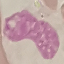

result = negative for malaria parasites
stain = Giemsa
image type = cell patch, automatically extracted from a larger field of view and resized to 64 × 64 pixels
preparation = thin blood film
capture = smartphone camera at the microscope eyepiece